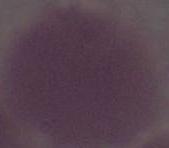
magnification = 1000x
modality = photomicrograph
identification = erythrocyte